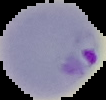

Image is 106×100 pixels. Segmented cell region on a black background. Malaria status: parasitized. From a thin blood smear.